Describe the morphology of the erythrocytes.
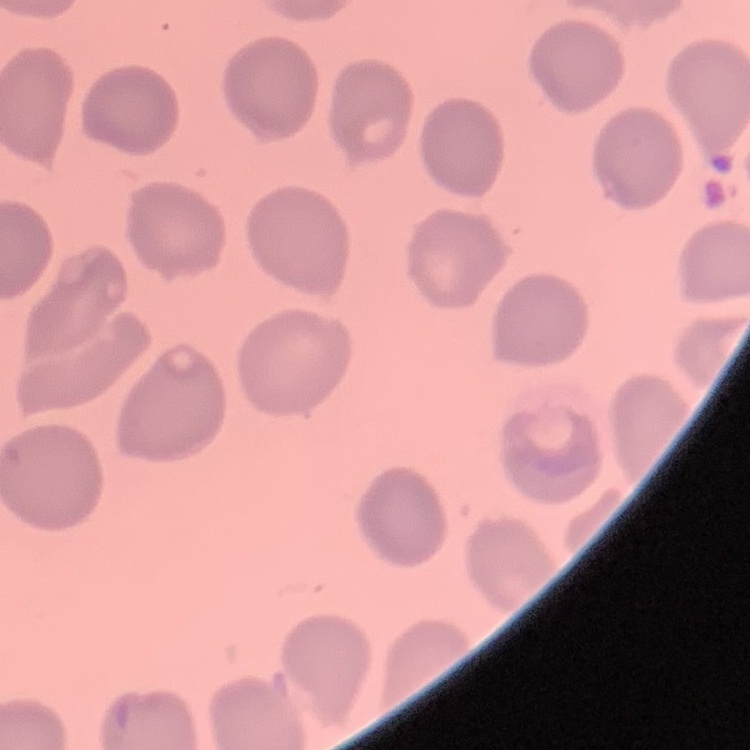

They show no rouleaux formation.

Thin peripheral smear. Square crop of a larger photomicrograph. Field's or Giemsa stain.